Classify this cell by malaria status.
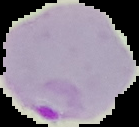

Parasitized.

Summary:
  - Preparation: thin blood film
  - Image size: 139×127 pixels
  - Image type: segmented cell region with the area outside set to black